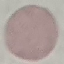
Summary:
  - Malaria status: uninfected
  - Stain: Giemsa
  - Image type: cell patch, automatically extracted from a larger field of view and resized to 64 × 64 pixels
  - Preparation: thin smear
  - Capture: smartphone camera at the microscope eyepiece